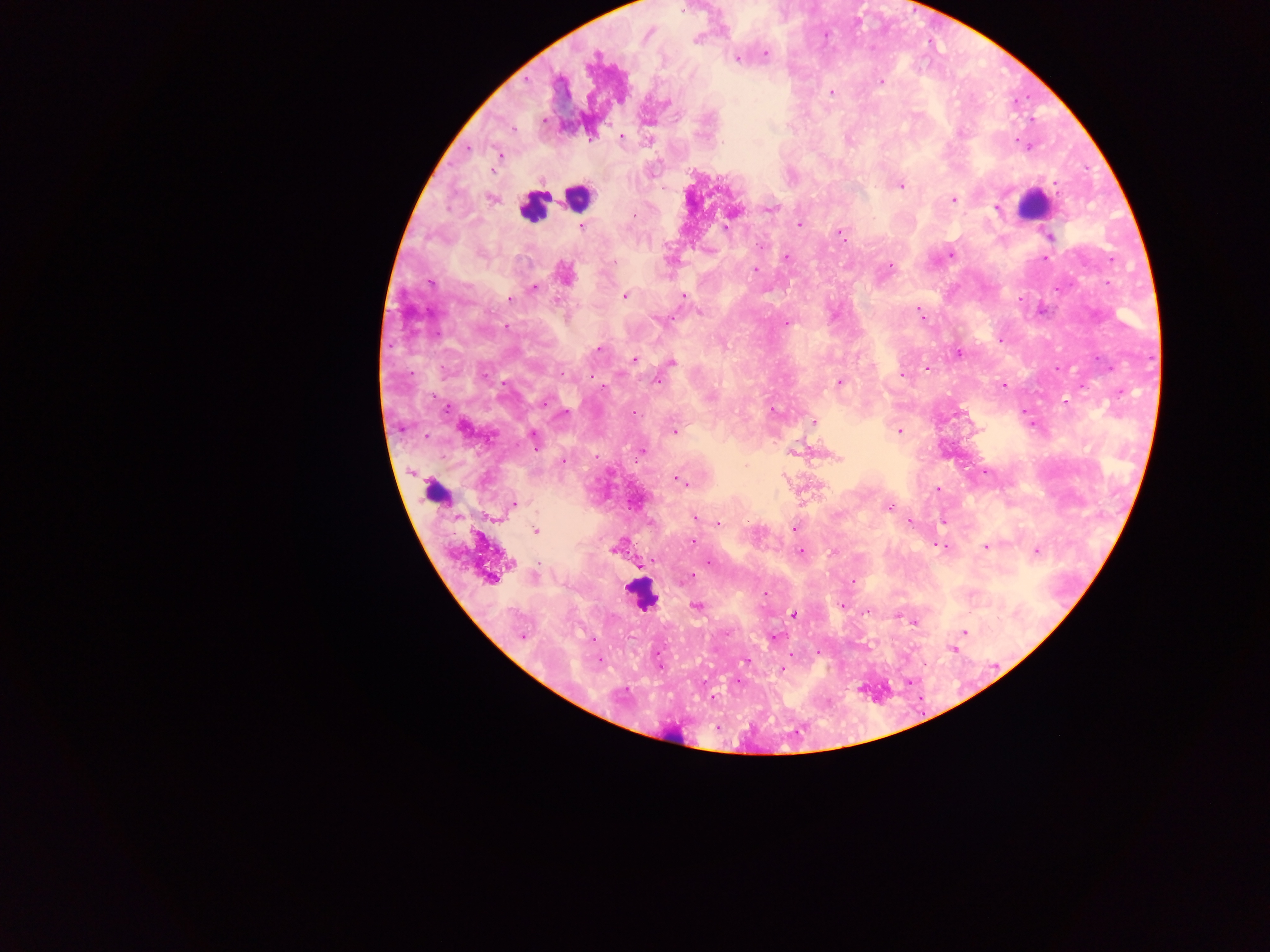

Approximate centers as (x, y) in pixels.
Summary:
  - Plasmodium parasite locations: (695, 40), (765, 54), (596, 55), (738, 58), (881, 81), (832, 92), (667, 103), (543, 120), (513, 129), (622, 137), (723, 142), (500, 155), (901, 186), (491, 198), (953, 199), (996, 208), (773, 209), (635, 216), (799, 224), (582, 226), (725, 226), (839, 232), (1050, 237), (762, 246), (950, 255), (787, 258), (1045, 258), (613, 262), (891, 265), (755, 269), (565, 273), (430, 284), (533, 288), (626, 295), (684, 296), (509, 298), (919, 310), (700, 312), (667, 319), (658, 320), (787, 323), (507, 326), (598, 349), (958, 353), (634, 360), (671, 362), (927, 368), (903, 374), (656, 380), (839, 382), (1003, 385), (604, 388), (1066, 402), (564, 413), (634, 413), (814, 422), (463, 428), (899, 430), (673, 432), (533, 439), (641, 452), (836, 457), (564, 461), (678, 479), (937, 489), (514, 504), (889, 508), (694, 518), (910, 522), (719, 523), (794, 528), (535, 531), (693, 541), (939, 545), (986, 546), (615, 548), (1036, 551), (800, 553), (708, 562), (490, 578), (688, 578), (853, 581), (842, 605), (697, 606), (867, 613), (794, 614), (913, 622), (965, 633), (522, 636), (774, 637), (819, 652), (599, 660), (746, 661), (782, 669)
  - Leukocyte locations: (577, 197), (1032, 206), (532, 207), (437, 490), (640, 594), (672, 734)
  - Country: Ghana
  - Image size: 1270×952 pixels
  - Field of view: single
  - Capture: mobile-phone photograph through a microscope
  - Preparation: thick blood film